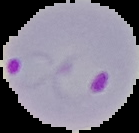

Malaria status: parasitized. Image is 139×133 pixels. Segmented cell region on a black background. From a thin blood smear.